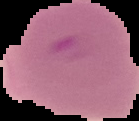

image size = 139×121 pixels
result = malaria parasites identified
preparation = thin blood film
image type = segmented cell region on a black background